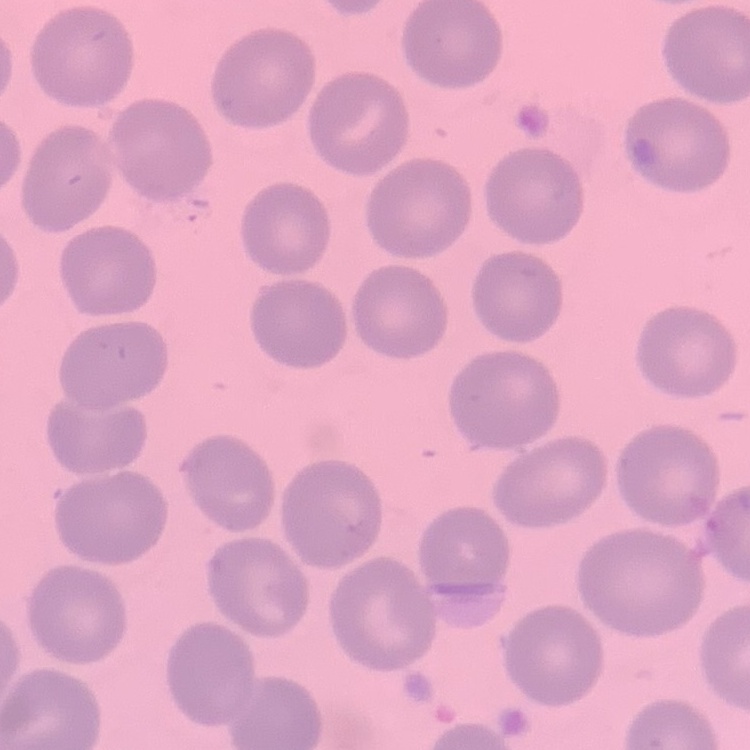
erythrocyte morphology = no rouleaux formation
preparation = thin blood smear
stain = Field's or Giemsa
image type = square crop of a larger photomicrograph